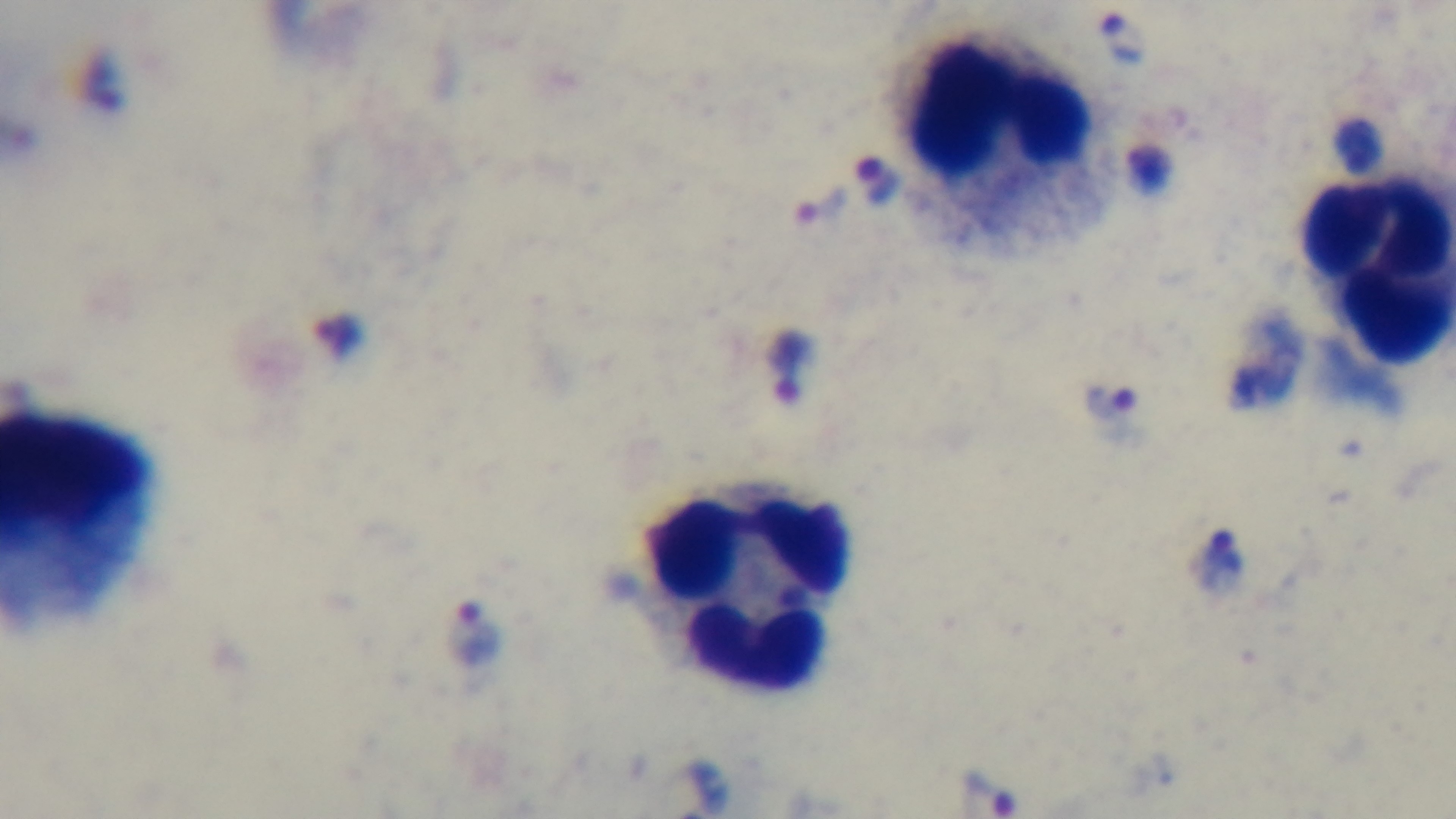
malaria status = positive
capture = mounted 4K digital camera
stain = Giemsa
preparation = thick blood film
modality = light microscopy
objective = 100x oil immersion
field of view = one from the slide